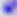

400x magnification. Micrograph. Toxoplasma gondii is seen.